Locate and identify every blood parasite.
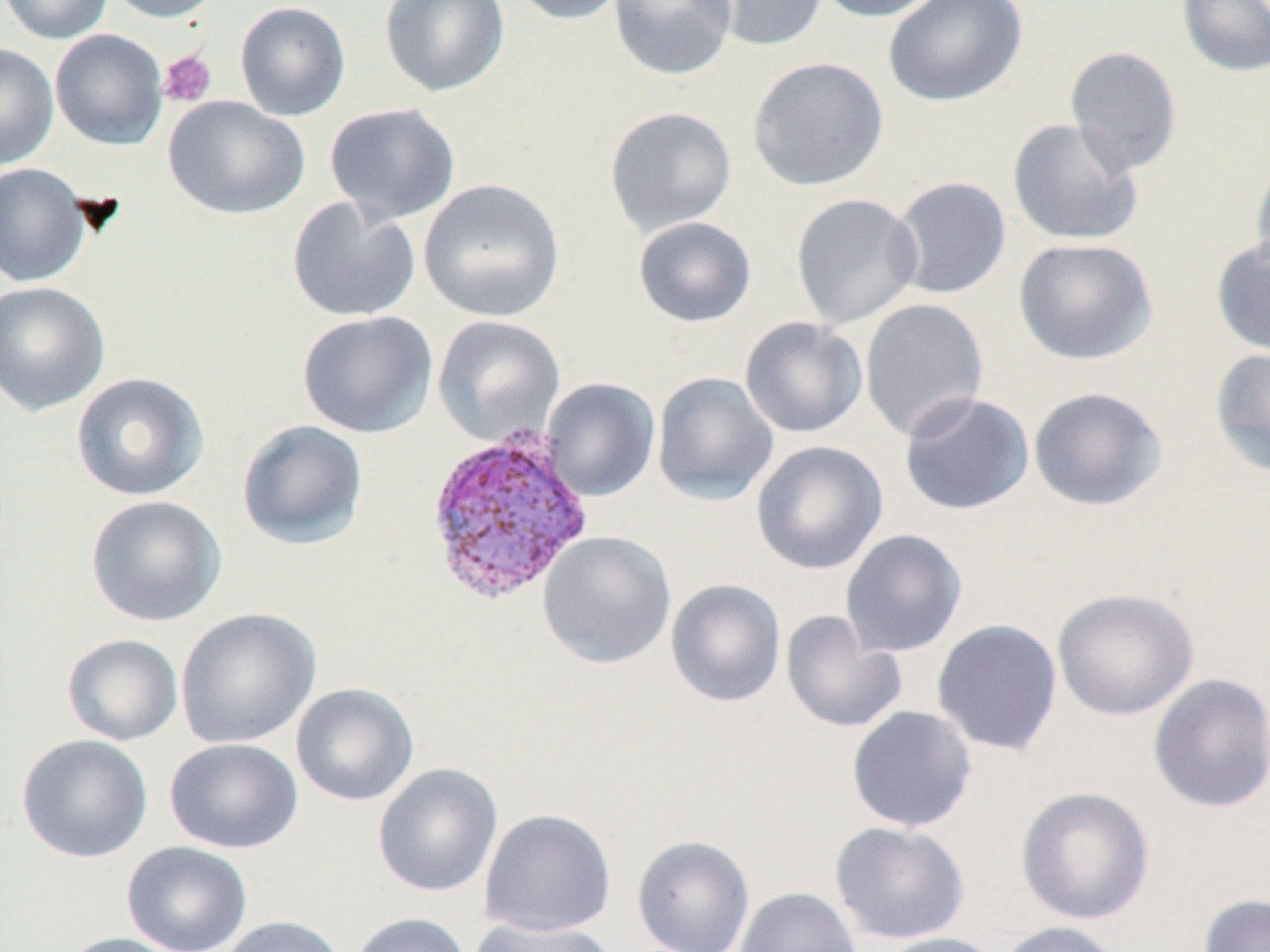
Approximate bounding boxes as (x1, y1, x2, y2) in pixels.
Plasmodium vivax-infected red blood cells: (424, 424, 595, 607).
No Plasmodium falciparum, Plasmodium ovale, Plasmodium malariae, Babesia divergens, or Trypanosoma brucei observed.

slide-level diagnosis = Plasmodium vivax
image size = 1270×952 pixels
magnification = 1000x
modality = light microscopy
field of view = one of a larger specimen
uninfected red blood cell locations = approximate bounding boxes as (x1, y1, x2, y2) in pixels: (0, 0, 113, 44), (106, 0, 225, 23), (234, 0, 351, 121), (379, 0, 510, 98), (508, 0, 629, 25), (609, 0, 737, 81), (698, 0, 830, 53), (811, 0, 947, 22), (883, 0, 1027, 107), (1176, 0, 1270, 78), (50, 29, 167, 150), (0, 44, 59, 169), (1065, 46, 1182, 174), (747, 56, 889, 191), (163, 95, 310, 220), (324, 102, 460, 225), (603, 106, 737, 237), (1007, 117, 1143, 246), (1250, 155, 1270, 281), (0, 162, 92, 287), (890, 176, 1012, 299), (418, 178, 565, 322), (791, 193, 923, 329), (286, 196, 420, 323), (633, 216, 757, 328), (1210, 237, 1270, 358), (1013, 238, 1158, 365), (0, 281, 111, 416), (859, 298, 989, 442), (297, 311, 438, 439), (432, 316, 565, 446), (739, 316, 868, 439), (1208, 346, 1270, 477), (70, 372, 210, 501), (652, 372, 778, 505), (541, 378, 660, 502), (1028, 386, 1168, 511), (898, 390, 1035, 516), (236, 419, 369, 550), (751, 440, 888, 575), (85, 495, 226, 627), (840, 529, 967, 657), (537, 531, 676, 668), (665, 579, 786, 707), (1051, 588, 1199, 721), (175, 608, 321, 749), (780, 610, 907, 733), (931, 619, 1063, 757), (61, 633, 183, 746), (1149, 672, 1270, 814), (291, 682, 419, 807), (846, 705, 978, 832), (16, 734, 154, 863), (165, 738, 303, 854), (372, 763, 503, 897), (1015, 785, 1155, 925), (479, 808, 616, 937), (830, 821, 969, 944), (632, 835, 755, 952), (121, 841, 253, 952), (734, 887, 861, 952), (1198, 893, 1270, 952), (348, 912, 473, 952), (217, 915, 348, 952), (468, 917, 618, 951), (997, 920, 1126, 952), (58, 932, 191, 952), (873, 932, 1008, 952)
stain = May-Grünwald-Giemsa
platelet locations = approximate bounding boxes as (x1, y1, x2, y2) in pixels: (158, 50, 217, 108)
preparation = thin blood film